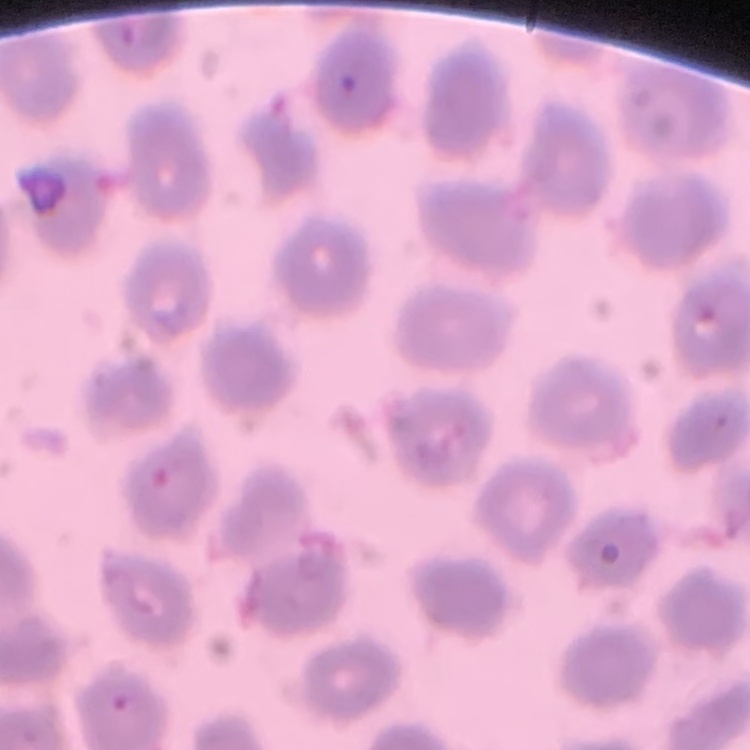
red blood cell morphology = no rouleaux formation
stain = Field's or Giemsa
preparation = thin peripheral smear
image type = square crop of a larger photomicrograph